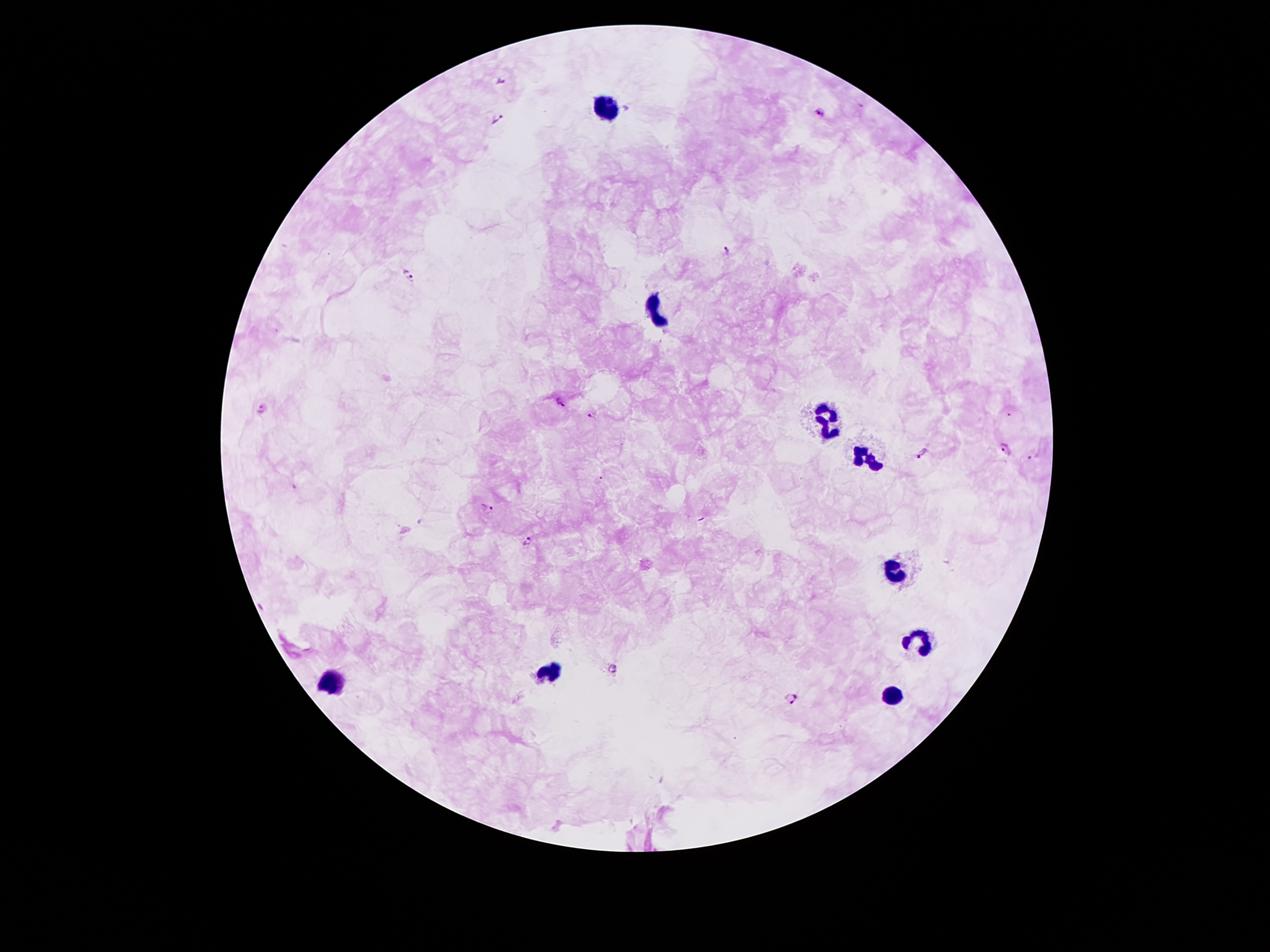 Approximate centers as {x, y} in pixels. Leukocyte locations: {607, 105}, {651, 310}, {827, 419}, {871, 453}, {896, 571}, {918, 643}, {545, 673}, {333, 681}, {893, 698}. Plasmodium parasite locations: {499, 80}, {820, 111}, {497, 121}, {728, 248}, {407, 274}, {560, 401}, {261, 409}, {593, 414}, {1005, 449}, {923, 455}, {1032, 458}, {486, 508}, {528, 541}, {612, 668}, {793, 699}. Giemsa-stained preparation. 100x magnification. Smartphone photograph taken through the microscope eyepiece. Image is 1270×952 pixels. Patient malaria status: infected with Plasmodium falciparum. Thick blood film. One field from this slide.